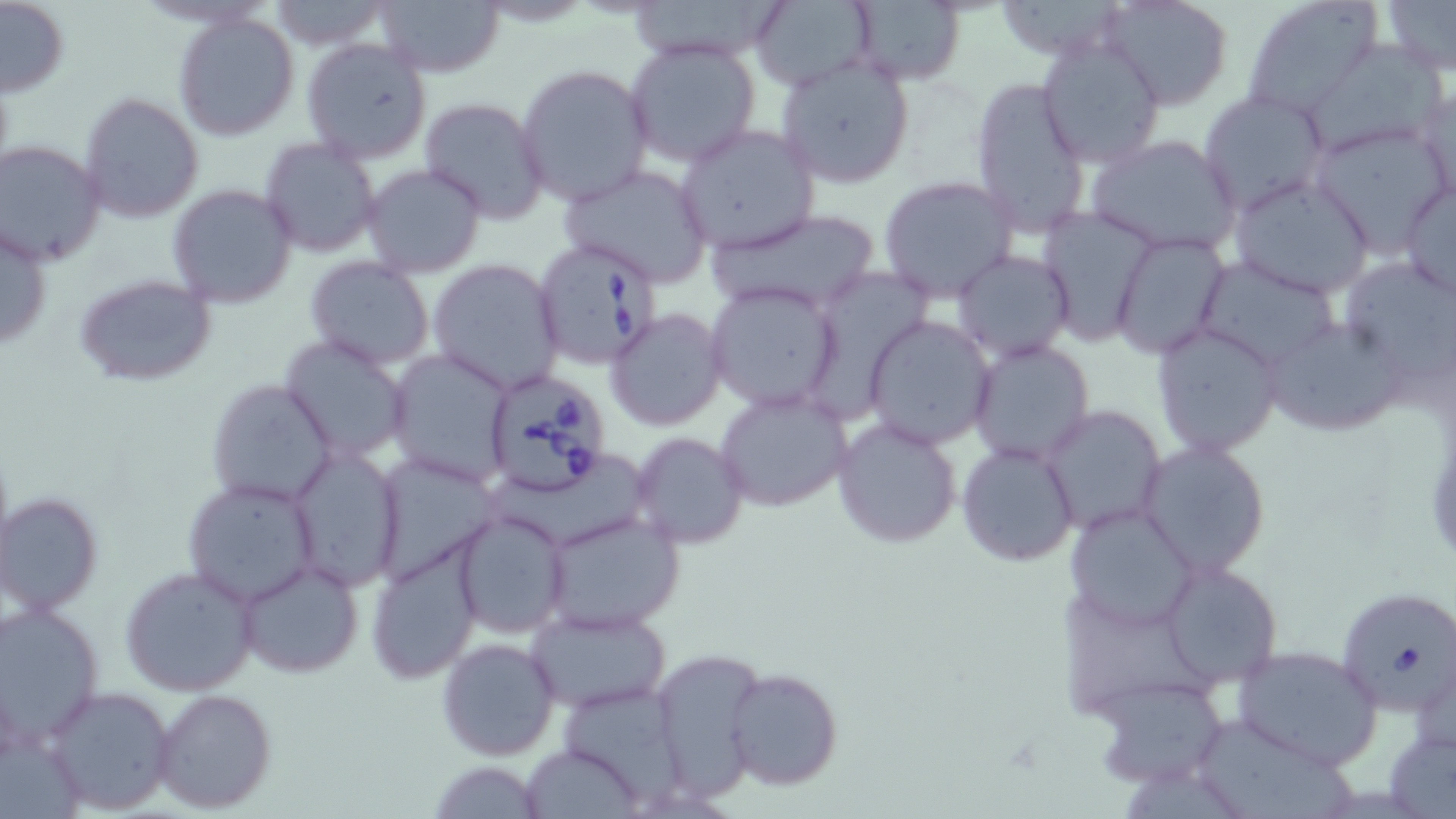
Approximate bounding boxes as (x1, y1, x2, y2) in pixels. Uninfected red blood cell locations: (0, 0, 69, 99), (625, 0, 794, 64), (748, 0, 877, 90), (1102, 0, 1233, 111), (1243, 0, 1384, 115), (1377, 0, 1456, 77), (267, 1, 390, 48), (373, 1, 506, 78), (843, 2, 968, 87), (173, 11, 301, 140), (1034, 33, 1166, 169), (625, 38, 762, 169), (301, 39, 432, 163), (1310, 43, 1446, 153), (776, 56, 916, 188), (515, 63, 654, 208), (969, 75, 1092, 238), (1416, 83, 1455, 208), (1197, 89, 1328, 213), (78, 92, 204, 224), (418, 96, 551, 224), (1307, 121, 1451, 257), (675, 124, 820, 253), (1086, 134, 1243, 257), (260, 137, 381, 258), (1, 139, 108, 266), (362, 163, 487, 279), (558, 165, 713, 287), (1228, 174, 1375, 299), (878, 176, 1019, 303), (1397, 180, 1456, 299), (168, 184, 299, 309), (701, 206, 884, 319), (1038, 207, 1160, 344), (1, 223, 53, 352), (1110, 232, 1230, 358), (953, 250, 1074, 361), (1192, 254, 1342, 371), (304, 257, 436, 371), (428, 258, 563, 394), (1353, 259, 1456, 377), (814, 269, 931, 424), (73, 273, 219, 389), (706, 282, 843, 413), (606, 308, 727, 430), (863, 314, 998, 448), (1257, 318, 1411, 438), (1152, 324, 1283, 457), (279, 335, 414, 461), (968, 339, 1094, 462), (387, 353, 516, 483), (205, 378, 339, 507), (716, 386, 852, 512), (1043, 405, 1167, 533), (832, 416, 962, 549), (631, 433, 747, 549), (958, 441, 1079, 566), (1139, 442, 1271, 577), (288, 446, 405, 591), (182, 477, 320, 607), (2, 492, 103, 617), (1063, 502, 1200, 631), (452, 507, 571, 638), (539, 510, 683, 633), (365, 540, 485, 685), (235, 559, 364, 678), (1160, 560, 1282, 686), (118, 564, 262, 698), (0, 604, 104, 745), (527, 605, 672, 713), (436, 636, 562, 760), (1229, 643, 1383, 769), (649, 649, 767, 795), (724, 668, 845, 790), (1091, 675, 1229, 788), (42, 685, 176, 815), (152, 687, 276, 814), (1188, 713, 1348, 819), (1383, 716, 1455, 817), (522, 744, 643, 818), (428, 761, 548, 817). Babesia divergens-infected red blood cell locations: (533, 238, 661, 368), (481, 367, 614, 497), (1336, 586, 1456, 714). Slide-level diagnosis: Babesia divergens. May-Grünwald-Giemsa stain. Captured at 1000x magnification. Single field of view. Image is 1456×819 pixels. Thin blood smear. Optical microscopy.